Classify this cell by malaria status.
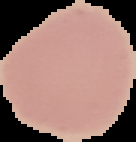
It is uninfected.

{
  "image_size": "136×142 pixels",
  "preparation": "thin blood smear",
  "image_type": "segmented cell region with the area outside set to black"
}